Assess this cell for malaria.
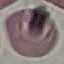

It is uninfected.

capture = smartphone camera at the microscope eyepiece
preparation = thin smear
stain = Giemsa
image type = cell patch, automatically extracted from a larger field of view and resized to 64 × 64 pixels